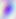
identification = Toxoplasma gondii
magnification = 400x
modality = micrograph